Classify this cell by malaria status.
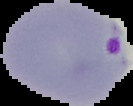
Parasitized.

Summary:
  - Image type: segmented cell region on a black background
  - Preparation: thin blood smear
  - Image size: 133×106 pixels